Outline each blood parasite and name the species.
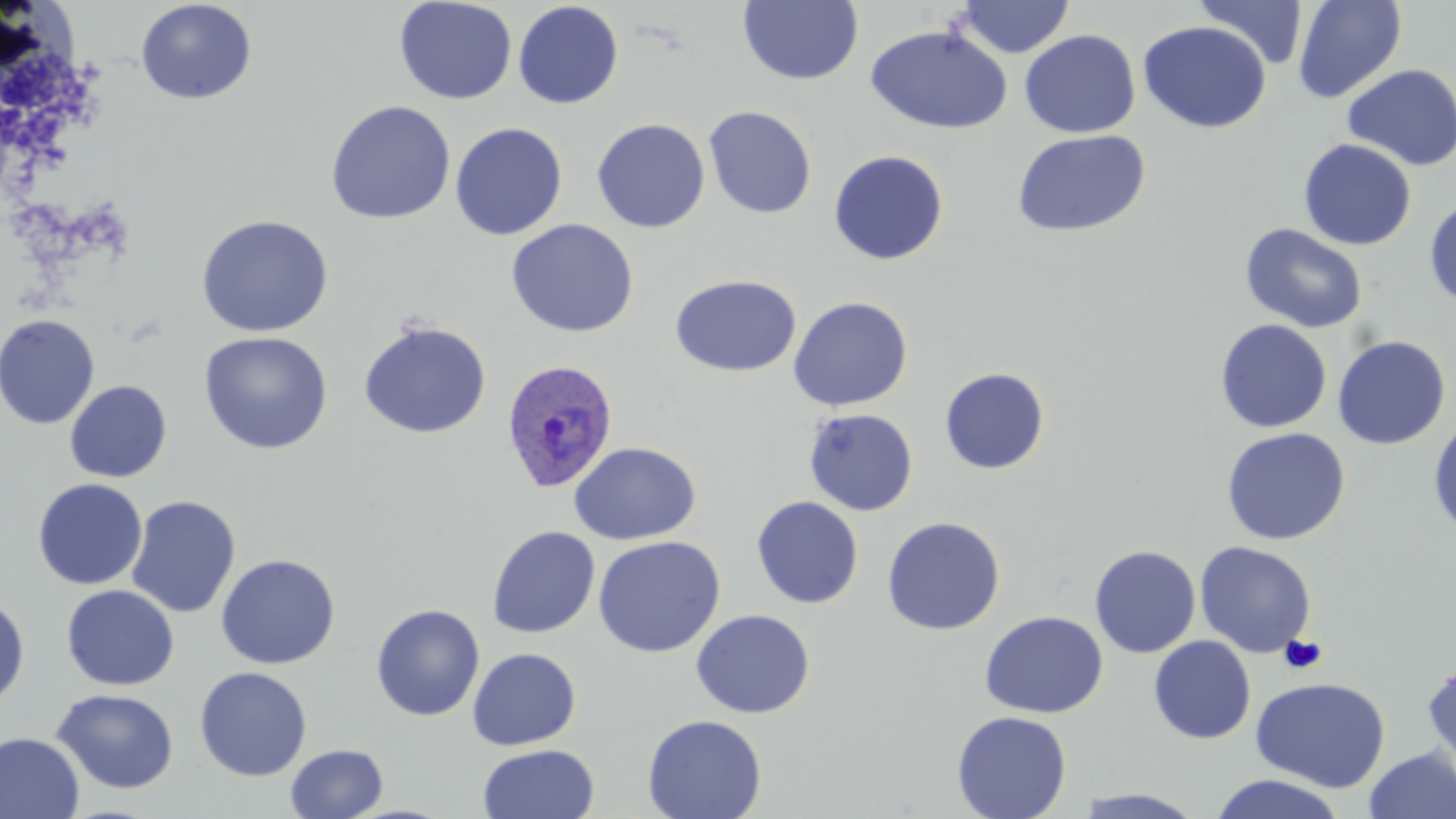
Approximate bounding boxes as (x1,y1)-(x2,y2) corner pairs in pixels.
Plasmodium ovale-infected red blood cells: (500,358)-(620,493).
No Plasmodium falciparum, Plasmodium malariae, Plasmodium vivax, Babesia divergens, or Trypanosoma brucei observed.

Summary:
  - Platelet locations: (1280,635)-(1327,674)
  - Uninfected red blood cell locations: (135,0)-(257,105), (394,0)-(517,104), (737,0)-(864,86), (954,0)-(1074,58), (1195,0)-(1311,70), (1292,0)-(1408,103), (513,2)-(624,109), (1137,20)-(1271,134), (865,24)-(1013,135), (1020,30)-(1141,138), (1342,63)-(1456,170), (325,100)-(456,225), (703,105)-(817,219), (591,118)-(711,233), (449,122)-(568,241), (1012,129)-(1151,237), (1298,138)-(1417,250), (828,150)-(949,266), (1424,197)-(1456,309), (196,214)-(333,337), (506,218)-(639,338), (1239,223)-(1369,334), (670,274)-(801,377), (788,296)-(913,411), (0,314)-(101,429), (1214,319)-(1332,433), (358,320)-(492,439), (198,331)-(333,455), (1332,334)-(1451,449), (939,367)-(1050,474), (64,380)-(172,483), (804,408)-(918,516), (1428,414)-(1456,539), (1220,427)-(1351,545), (569,441)-(701,546), (32,478)-(148,590), (126,496)-(241,618), (751,496)-(864,609), (881,515)-(1005,635), (486,525)-(600,638), (592,536)-(725,657), (1195,541)-(1317,658), (1089,545)-(1201,658), (215,553)-(341,669), (61,585)-(180,691), (0,593)-(30,709), (370,603)-(485,721), (691,609)-(815,718), (979,610)-(1108,718), (1149,636)-(1256,744), (466,647)-(581,750), (1421,660)-(1456,778), (194,666)-(312,780), (1251,677)-(1390,793), (51,688)-(179,794), (952,711)-(1072,819), (642,713)-(767,819), (0,732)-(84,819), (285,743)-(388,818), (478,743)-(600,819), (1363,747)-(1456,819), (1209,773)-(1347,819), (1075,788)-(1208,818)
  - Slide-level diagnosis: Plasmodium ovale
  - Magnification: 1000x
  - Preparation: thin blood film
  - Field of view: single
  - Modality: light microscopy
  - Image size: 1456×819 pixels
  - Stain: May-Grünwald-Giemsa